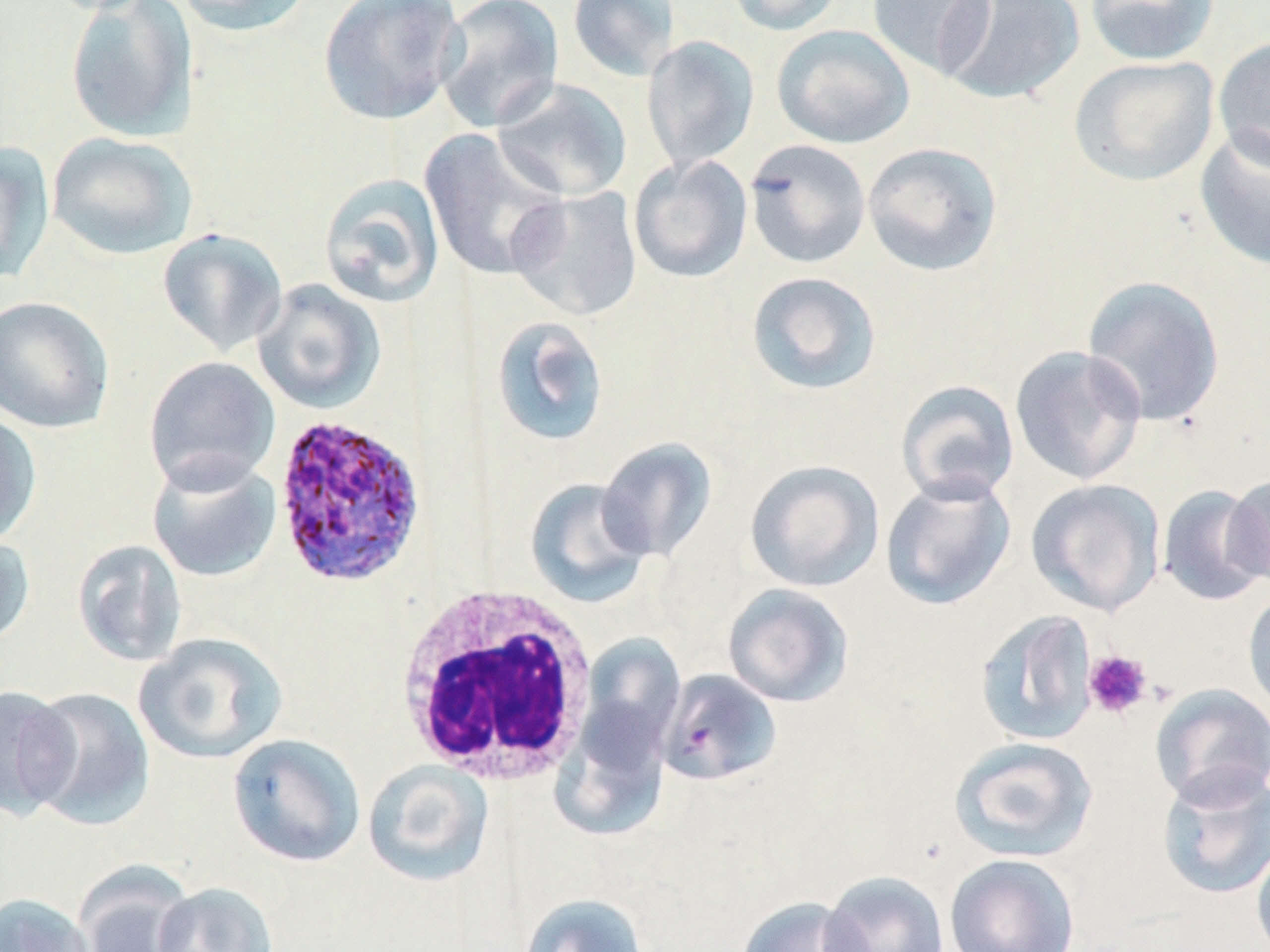 Approximate bounding boxes as (x1,y1)-(x2,y2) corner pairs in pixels. Platelet locations: (1082,649)-(1152,720). White blood cell locations: (394,586)-(599,786). Plasmodium ovale-infected red blood cell locations: (272,412)-(427,587). Uninfected red blood cell locations: (39,0)-(158,15), (64,0)-(198,143), (169,0)-(316,37), (318,0)-(464,125), (433,0)-(564,134), (566,0)-(680,83), (724,0)-(845,36), (866,0)-(996,78), (937,0)-(1086,105), (1083,0)-(1220,66), (772,24)-(915,149), (641,35)-(760,171), (1213,36)-(1270,172), (1069,55)-(1220,187), (492,78)-(632,202), (1194,125)-(1270,271), (418,128)-(569,282), (46,132)-(197,260), (743,139)-(871,269), (0,141)-(54,285), (862,142)-(1002,276), (628,154)-(753,283), (319,172)-(445,308), (507,186)-(643,322), (157,227)-(288,358), (745,271)-(882,395), (1081,275)-(1226,426), (252,279)-(386,414), (0,295)-(115,434), (489,316)-(610,447), (1010,345)-(1147,485), (143,356)-(280,494), (896,380)-(1019,506), (0,408)-(42,548), (596,437)-(718,562), (147,454)-(282,583), (745,459)-(885,593), (1224,472)-(1270,589), (880,474)-(1016,610), (524,478)-(655,608), (1026,478)-(1166,617), (1158,484)-(1269,607), (0,531)-(35,652), (72,538)-(188,667), (722,583)-(854,707), (1242,586)-(1270,717), (974,610)-(1099,747), (132,632)-(288,764), (578,634)-(685,754), (655,668)-(780,786), (1150,684)-(1270,809), (0,685)-(79,821), (21,687)-(156,830), (549,694)-(673,842), (227,733)-(365,867), (949,737)-(1098,862), (363,760)-(495,887), (1156,765)-(1270,900), (1251,837)-(1270,952), (944,853)-(1080,952), (74,864)-(196,951), (819,870)-(950,952), (153,882)-(279,952), (0,892)-(96,952), (519,893)-(648,952), (736,896)-(868,952). Slide-level diagnosis: Plasmodium ovale. 1000x magnification. Image is 1270×952 pixels. Optical microscopy. Thin blood film. Single field of view. May-Grünwald-Giemsa stain.